Identify the parasite.
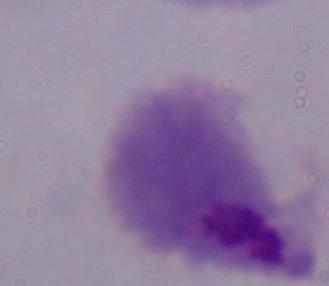
This is a trichomonad.

Summary:
  - Magnification: 1000x
  - Modality: photomicrograph